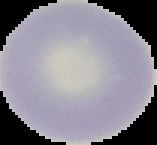 Segmented cell region on a black background. Image is 157×145 pixels. Result: no malaria parasites seen. From a thin blood film.